Locate every blood parasite and identify its species.
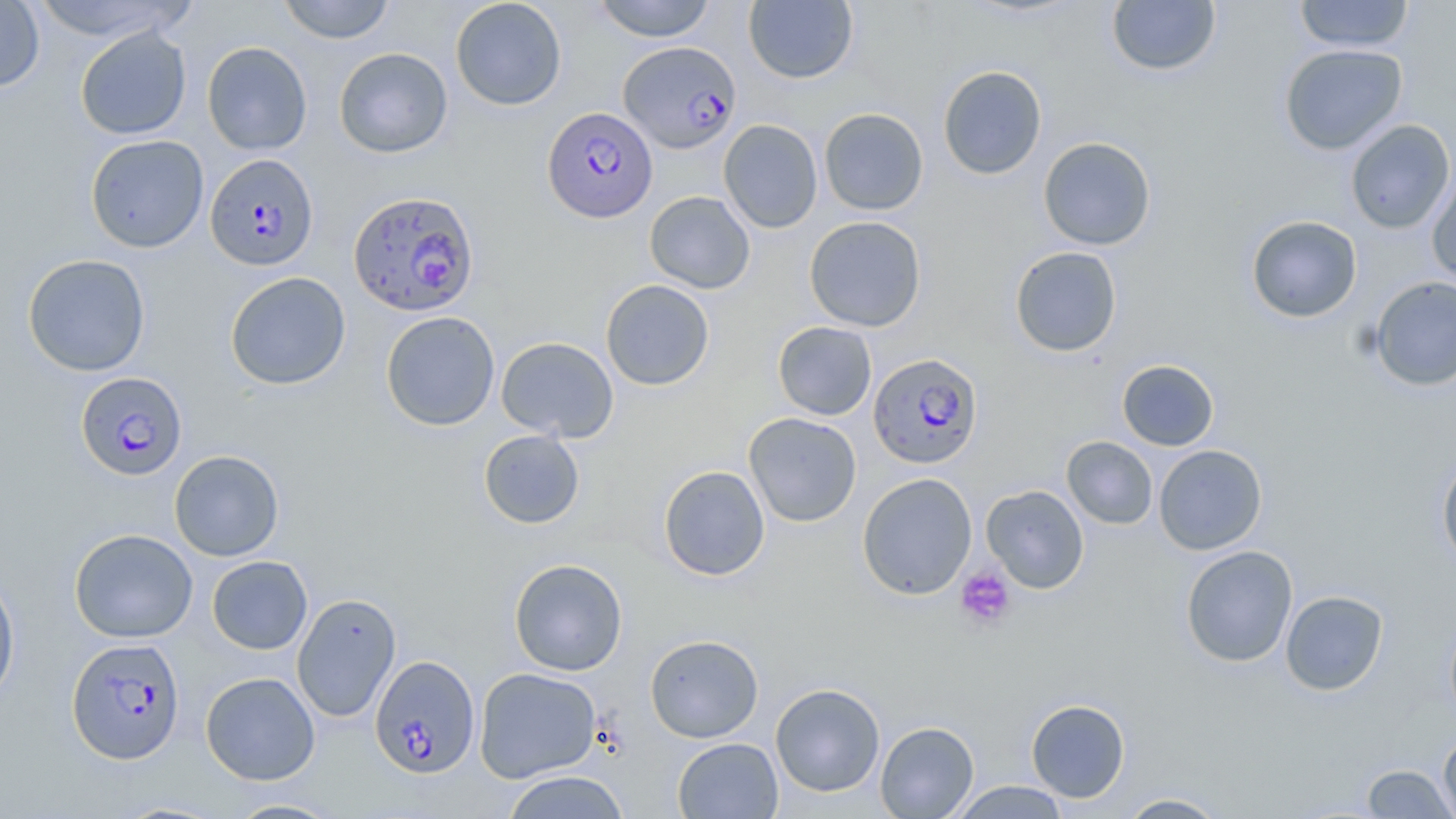

Approximate bounding boxes as named x1/y1/x2/y2 corners in pixels.
Plasmodium falciparum-infected red blood cells: (x1=615, y1=43, x2=738, y2=156), (x1=542, y1=106, x2=657, y2=222), (x1=205, y1=153, x2=319, y2=272), (x1=348, y1=189, x2=479, y2=317), (x1=867, y1=352, x2=983, y2=470), (x1=75, y1=372, x2=187, y2=480), (x1=66, y1=638, x2=185, y2=764), (x1=369, y1=655, x2=480, y2=778).
No Plasmodium ovale, Plasmodium malariae, Plasmodium vivax, Babesia divergens, or Trypanosoma brucei observed.

Uninfected red blood cell locations: (x1=28, y1=0, x2=190, y2=42), (x1=277, y1=0, x2=395, y2=44), (x1=450, y1=0, x2=567, y2=110), (x1=592, y1=0, x2=717, y2=42), (x1=743, y1=0, x2=858, y2=84), (x1=1105, y1=0, x2=1222, y2=77), (x1=1293, y1=0, x2=1415, y2=53), (x1=0, y1=1, x2=45, y2=92), (x1=74, y1=26, x2=192, y2=140), (x1=201, y1=41, x2=312, y2=155), (x1=1279, y1=43, x2=1408, y2=155), (x1=334, y1=47, x2=453, y2=158), (x1=937, y1=65, x2=1048, y2=179), (x1=818, y1=108, x2=929, y2=215), (x1=718, y1=119, x2=823, y2=233), (x1=1345, y1=120, x2=1455, y2=234), (x1=85, y1=134, x2=209, y2=253), (x1=1038, y1=136, x2=1156, y2=250), (x1=1427, y1=171, x2=1456, y2=289), (x1=644, y1=191, x2=755, y2=294), (x1=804, y1=215, x2=927, y2=332), (x1=1246, y1=215, x2=1362, y2=323), (x1=1009, y1=246, x2=1123, y2=357), (x1=22, y1=254, x2=151, y2=377), (x1=224, y1=271, x2=351, y2=390), (x1=1369, y1=276, x2=1456, y2=391), (x1=600, y1=279, x2=714, y2=390), (x1=380, y1=311, x2=500, y2=431), (x1=772, y1=321, x2=877, y2=420), (x1=496, y1=336, x2=619, y2=442), (x1=1117, y1=359, x2=1219, y2=451), (x1=743, y1=412, x2=861, y2=527), (x1=478, y1=429, x2=585, y2=529), (x1=1061, y1=436, x2=1158, y2=529), (x1=1153, y1=444, x2=1267, y2=555), (x1=169, y1=449, x2=284, y2=561), (x1=1436, y1=454, x2=1456, y2=571), (x1=658, y1=465, x2=770, y2=581), (x1=856, y1=472, x2=978, y2=600), (x1=981, y1=485, x2=1090, y2=594), (x1=69, y1=528, x2=198, y2=643), (x1=1180, y1=545, x2=1298, y2=668), (x1=206, y1=555, x2=312, y2=655), (x1=508, y1=558, x2=628, y2=676), (x1=0, y1=571, x2=20, y2=708), (x1=1280, y1=590, x2=1388, y2=695), (x1=291, y1=592, x2=402, y2=723), (x1=1444, y1=613, x2=1456, y2=729), (x1=645, y1=634, x2=764, y2=743), (x1=474, y1=667, x2=601, y2=782), (x1=200, y1=671, x2=320, y2=785), (x1=770, y1=683, x2=885, y2=797), (x1=1025, y1=699, x2=1130, y2=802), (x1=875, y1=721, x2=979, y2=818), (x1=1438, y1=730, x2=1456, y2=819), (x1=672, y1=737, x2=783, y2=818), (x1=1360, y1=763, x2=1455, y2=818), (x1=500, y1=771, x2=631, y2=818), (x1=949, y1=781, x2=1071, y2=818), (x1=1116, y1=793, x2=1230, y2=818), (x1=225, y1=798, x2=344, y2=818). Platelet locations: (x1=955, y1=566, x2=1016, y2=630). Slide-level diagnosis: Plasmodium falciparum. Optical microscopy. Image is 1456×819 pixels. Single field of view. Captured at 1000x magnification. Thin blood smear. May-Grünwald-Giemsa-stained preparation.